Report the malaria status of this cell.
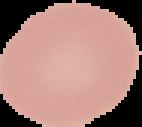
It is uninfected.

Summary:
  - Preparation: thin blood smear
  - Image type: segmented cell region with the area outside set to black
  - Image size: 142×127 pixels